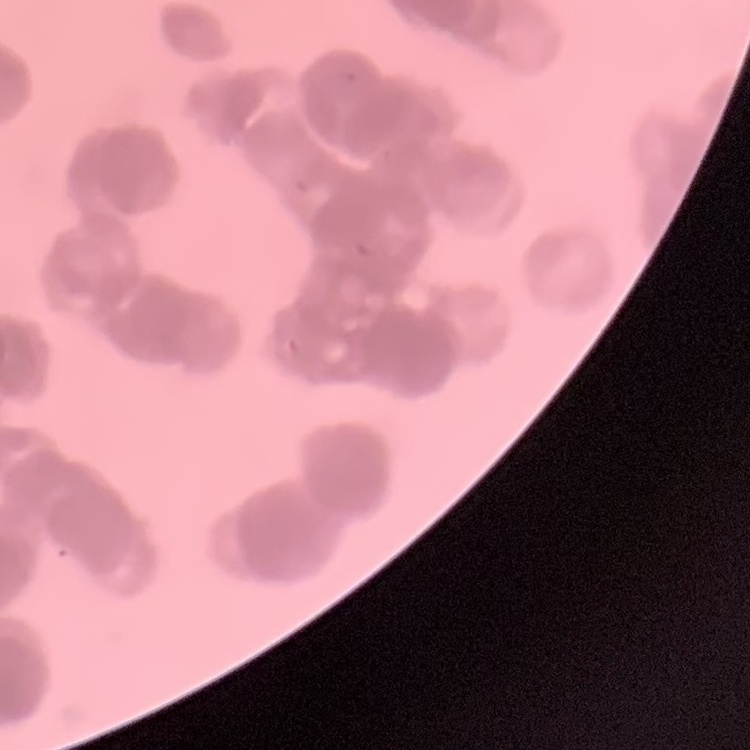

red blood cell morphology = rouleaux formation
stain = Field's or Giemsa
image type = one tile cut from a larger photomicrograph
preparation = thin blood smear